Identify the blood parasite species.
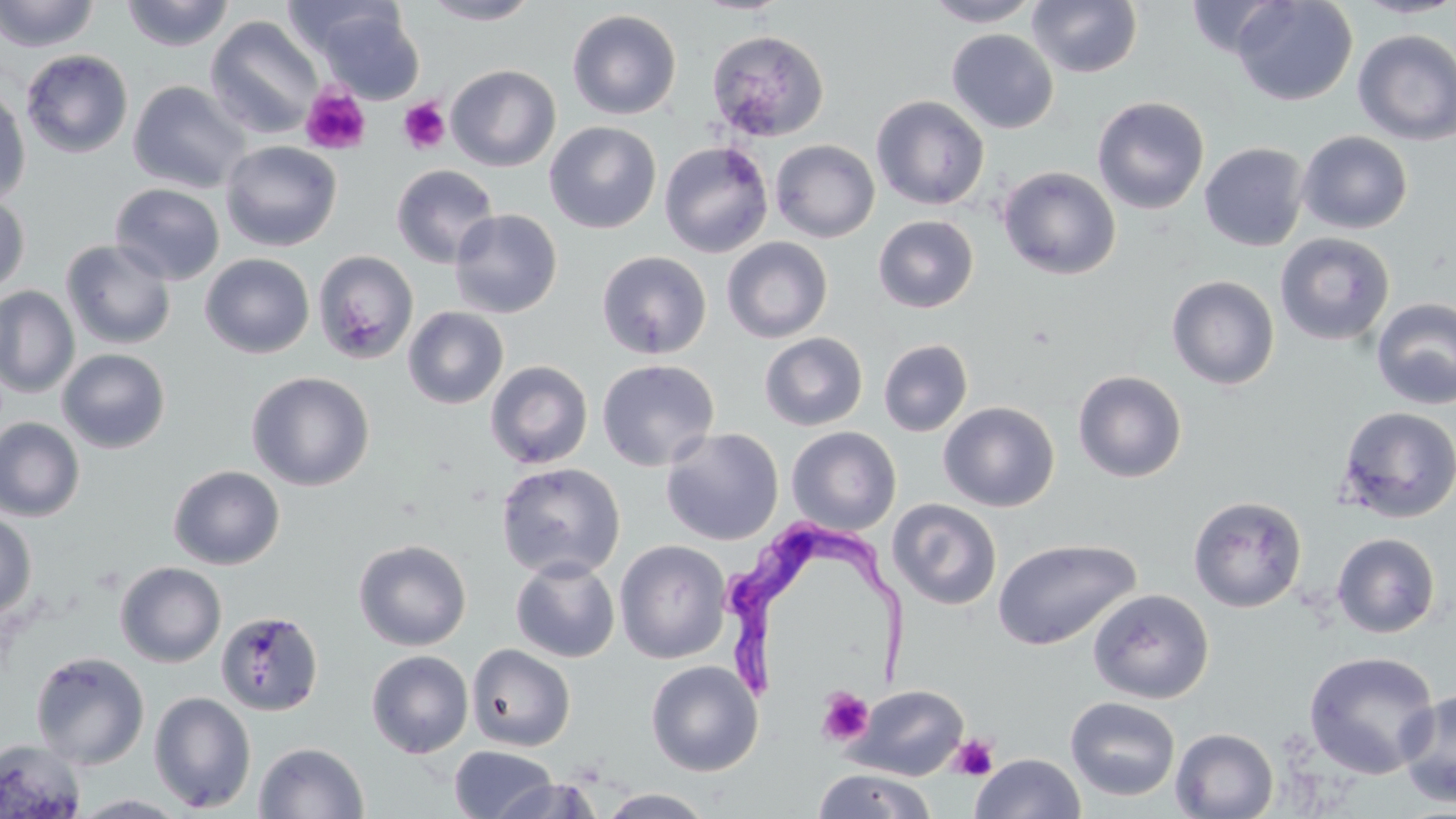
Trypanosoma brucei.

Approximate bounding boxes as [x1, y1, x2, y2] in pixels. Uninfected red blood cell locations: [0, 0, 100, 52], [120, 0, 235, 51], [421, 0, 540, 25], [923, 0, 1042, 27], [1027, 0, 1143, 78], [1231, 0, 1358, 106], [1351, 0, 1456, 19], [311, 4, 425, 104], [567, 9, 682, 120], [205, 16, 323, 139], [946, 28, 1059, 134], [706, 29, 830, 142], [1353, 29, 1456, 145], [21, 49, 133, 159], [446, 64, 561, 171], [128, 80, 252, 194], [0, 83, 31, 208], [871, 95, 990, 210], [1092, 96, 1210, 215], [544, 121, 662, 234], [1296, 130, 1413, 234], [770, 139, 880, 242], [220, 140, 342, 252], [659, 141, 774, 258], [1199, 142, 1309, 252], [391, 164, 499, 268], [998, 166, 1121, 280], [109, 183, 225, 285], [0, 192, 30, 297], [449, 208, 563, 318], [873, 214, 979, 313], [1275, 232, 1395, 346], [721, 237, 833, 343], [61, 239, 177, 349], [313, 250, 419, 365], [596, 251, 712, 360], [200, 253, 315, 359], [1166, 275, 1280, 390], [0, 286, 80, 398], [1371, 297, 1456, 410], [403, 306, 509, 409], [759, 332, 868, 432], [878, 339, 973, 436], [57, 348, 170, 453], [596, 359, 720, 472], [485, 360, 594, 470], [1072, 370, 1187, 483], [246, 371, 374, 491], [938, 401, 1060, 512], [1335, 405, 1456, 524], [0, 417, 85, 522], [786, 426, 901, 535], [660, 427, 784, 546], [495, 461, 626, 581], [168, 464, 285, 570], [1188, 495, 1307, 613], [887, 498, 1003, 611], [0, 511, 37, 621], [1332, 532, 1441, 638], [991, 538, 1141, 651], [353, 539, 472, 651], [614, 540, 732, 664], [510, 557, 620, 663], [115, 562, 227, 667], [1088, 588, 1214, 704], [215, 610, 324, 716], [466, 644, 576, 752], [366, 650, 474, 758], [30, 651, 150, 769], [1303, 651, 1440, 779], [646, 660, 763, 777], [846, 684, 970, 780], [1397, 689, 1456, 809], [148, 691, 257, 813], [1065, 696, 1181, 801], [1170, 727, 1279, 819], [0, 739, 86, 818], [254, 742, 370, 819], [449, 744, 559, 819], [970, 753, 1086, 819], [811, 768, 938, 819], [493, 777, 605, 819], [597, 788, 715, 818], [70, 794, 193, 818]. Platelet locations: [300, 84, 371, 155], [399, 97, 451, 155], [817, 687, 874, 746], [948, 734, 999, 781]. Trypanosoma brucei locations: [712, 519, 909, 699]. Image is 1456×819 pixels. Captured at 1000x magnification. Light microscopy. Thin blood smear. One field of a larger specimen. May-Grünwald-Giemsa-stained preparation.